Identify the cell.
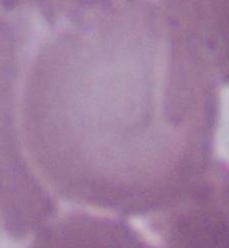
An erythrocyte.

magnification = 1000x
modality = photomicrograph